Report the malaria status of this cell.
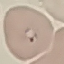

It is parasitized.

{
  "preparation": "thin smear",
  "capture": "smartphone through the microscope eyepiece",
  "image_type": "automatically extracted cell patch, resized to 64 × 64 pixels",
  "stain": "Giemsa"
}